Comment on the morphology of the red blood cells.
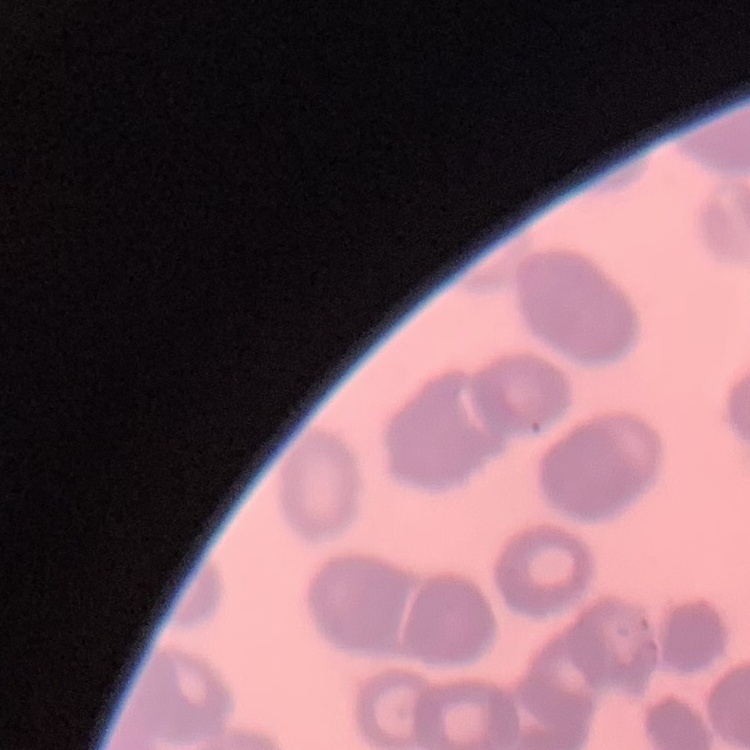
They show rouleaux formation.

Summary:
  - Stain: Field's or Giemsa
  - Image type: one tile cut from a larger photomicrograph
  - Preparation: thin peripheral smear